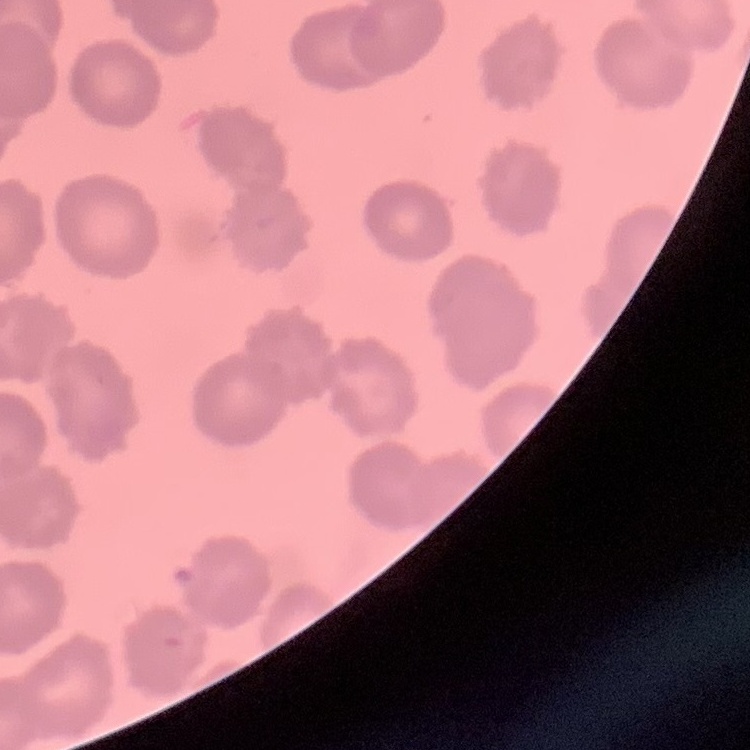

Summary:
  - Red blood cell morphology: no rouleaux formation
  - Image type: square crop of a larger photomicrograph
  - Preparation: thin blood smear
  - Stain: Field's or Giemsa